Outline each Trypanosoma brucei.
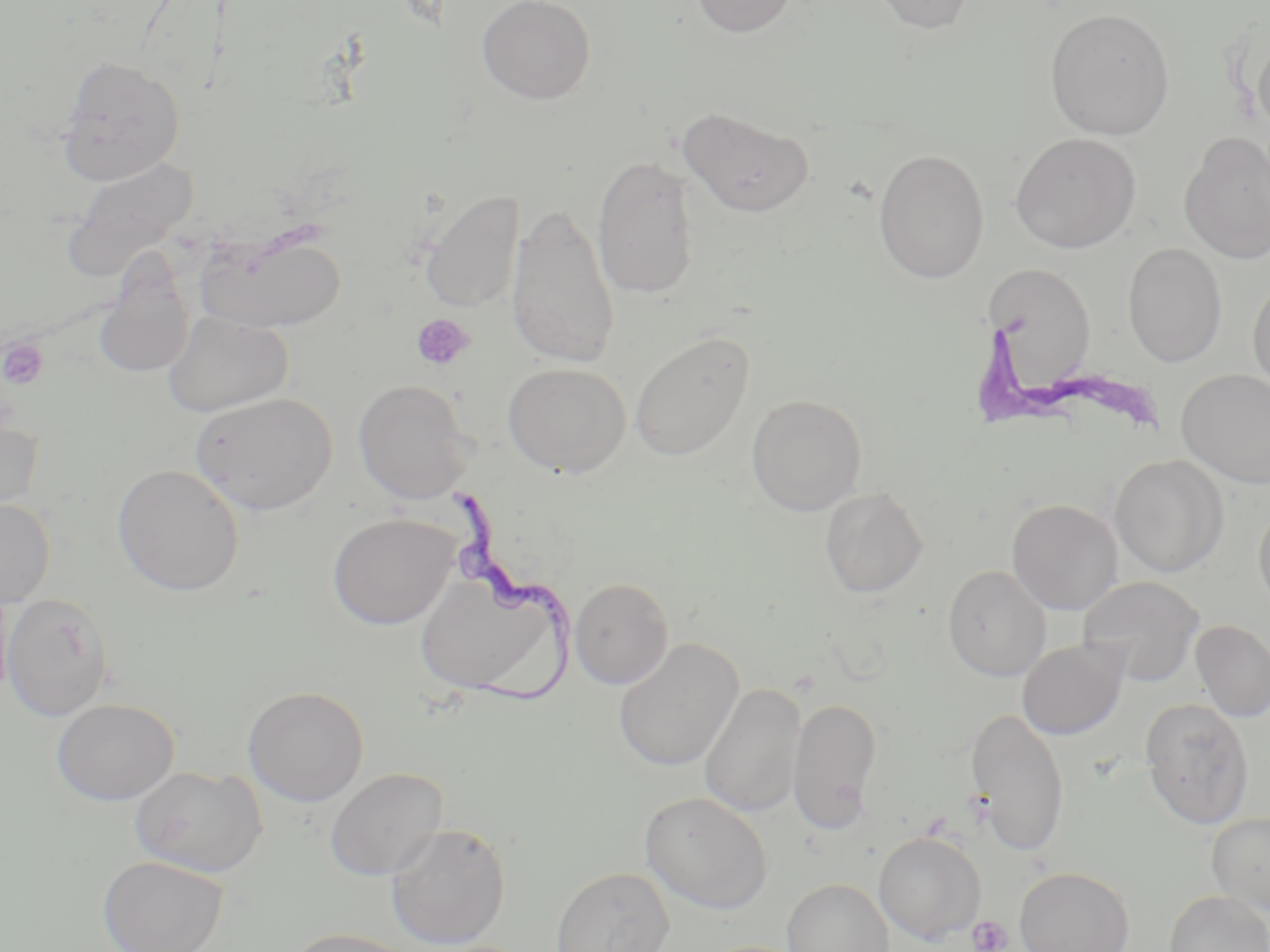
Approximate bounding boxes as named x1/y1/x2/y2 corners in pixels.
Trypanosoma brucei: (x1=446, y1=485, x2=577, y2=705).

Platelet locations: (x1=412, y1=314, x2=475, y2=371), (x1=1, y1=338, x2=48, y2=390), (x1=967, y1=914, x2=1014, y2=952). Uninfected red blood cell locations: (x1=477, y1=0, x2=596, y2=104), (x1=688, y1=0, x2=802, y2=38), (x1=867, y1=0, x2=980, y2=35), (x1=1044, y1=8, x2=1175, y2=140), (x1=1252, y1=28, x2=1270, y2=140), (x1=57, y1=54, x2=186, y2=185), (x1=677, y1=105, x2=815, y2=218), (x1=1179, y1=131, x2=1270, y2=264), (x1=1010, y1=132, x2=1142, y2=253), (x1=873, y1=149, x2=990, y2=283), (x1=62, y1=155, x2=201, y2=282), (x1=591, y1=155, x2=702, y2=300), (x1=421, y1=190, x2=525, y2=312), (x1=506, y1=203, x2=620, y2=370), (x1=196, y1=227, x2=346, y2=334), (x1=1122, y1=242, x2=1227, y2=367), (x1=983, y1=260, x2=1097, y2=388), (x1=94, y1=261, x2=197, y2=379), (x1=1247, y1=275, x2=1270, y2=396), (x1=163, y1=310, x2=293, y2=417), (x1=629, y1=330, x2=756, y2=462), (x1=503, y1=362, x2=631, y2=477), (x1=1177, y1=369, x2=1270, y2=488), (x1=353, y1=379, x2=473, y2=504), (x1=190, y1=391, x2=337, y2=515), (x1=746, y1=394, x2=868, y2=515), (x1=0, y1=407, x2=43, y2=522), (x1=1109, y1=454, x2=1229, y2=577), (x1=113, y1=465, x2=244, y2=597), (x1=820, y1=486, x2=928, y2=598), (x1=0, y1=497, x2=55, y2=608), (x1=1007, y1=499, x2=1123, y2=615), (x1=1253, y1=500, x2=1270, y2=615), (x1=328, y1=513, x2=457, y2=630), (x1=942, y1=564, x2=1051, y2=681), (x1=415, y1=569, x2=571, y2=701), (x1=1078, y1=575, x2=1204, y2=685), (x1=569, y1=577, x2=674, y2=689), (x1=0, y1=580, x2=14, y2=704), (x1=2, y1=592, x2=114, y2=721), (x1=1191, y1=620, x2=1270, y2=722), (x1=613, y1=637, x2=743, y2=773), (x1=1017, y1=638, x2=1129, y2=740), (x1=698, y1=682, x2=808, y2=818), (x1=243, y1=685, x2=369, y2=806), (x1=787, y1=697, x2=884, y2=835), (x1=1140, y1=697, x2=1255, y2=829), (x1=51, y1=698, x2=179, y2=805), (x1=965, y1=707, x2=1070, y2=857), (x1=130, y1=765, x2=267, y2=877), (x1=325, y1=766, x2=449, y2=880), (x1=640, y1=791, x2=773, y2=915), (x1=1206, y1=812, x2=1270, y2=915), (x1=386, y1=823, x2=512, y2=949), (x1=874, y1=831, x2=986, y2=943), (x1=97, y1=855, x2=228, y2=952), (x1=551, y1=866, x2=675, y2=952), (x1=1015, y1=866, x2=1134, y2=952), (x1=781, y1=878, x2=894, y2=952), (x1=1164, y1=890, x2=1270, y2=952), (x1=283, y1=927, x2=423, y2=952). Slide-level diagnosis: Trypanosoma brucei. Thin blood smear. 1000x magnification. Optical microscopy. One field of a larger specimen. May-Grünwald-Giemsa-stained preparation. Image is 1270×952 pixels.